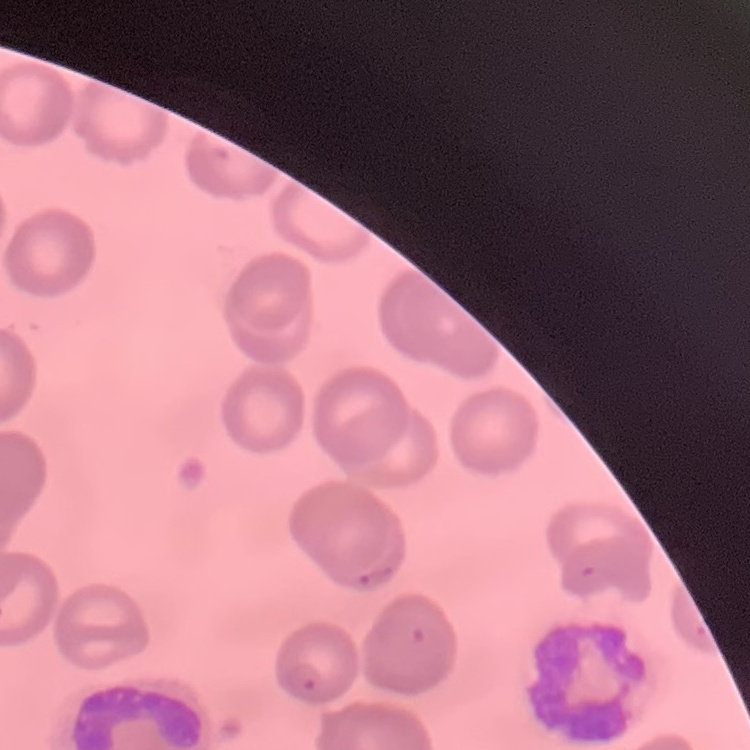
The red blood cells exhibit no rouleaux formation. Square crop of a larger photomicrograph. Field's or Giemsa stain. Thin blood film.